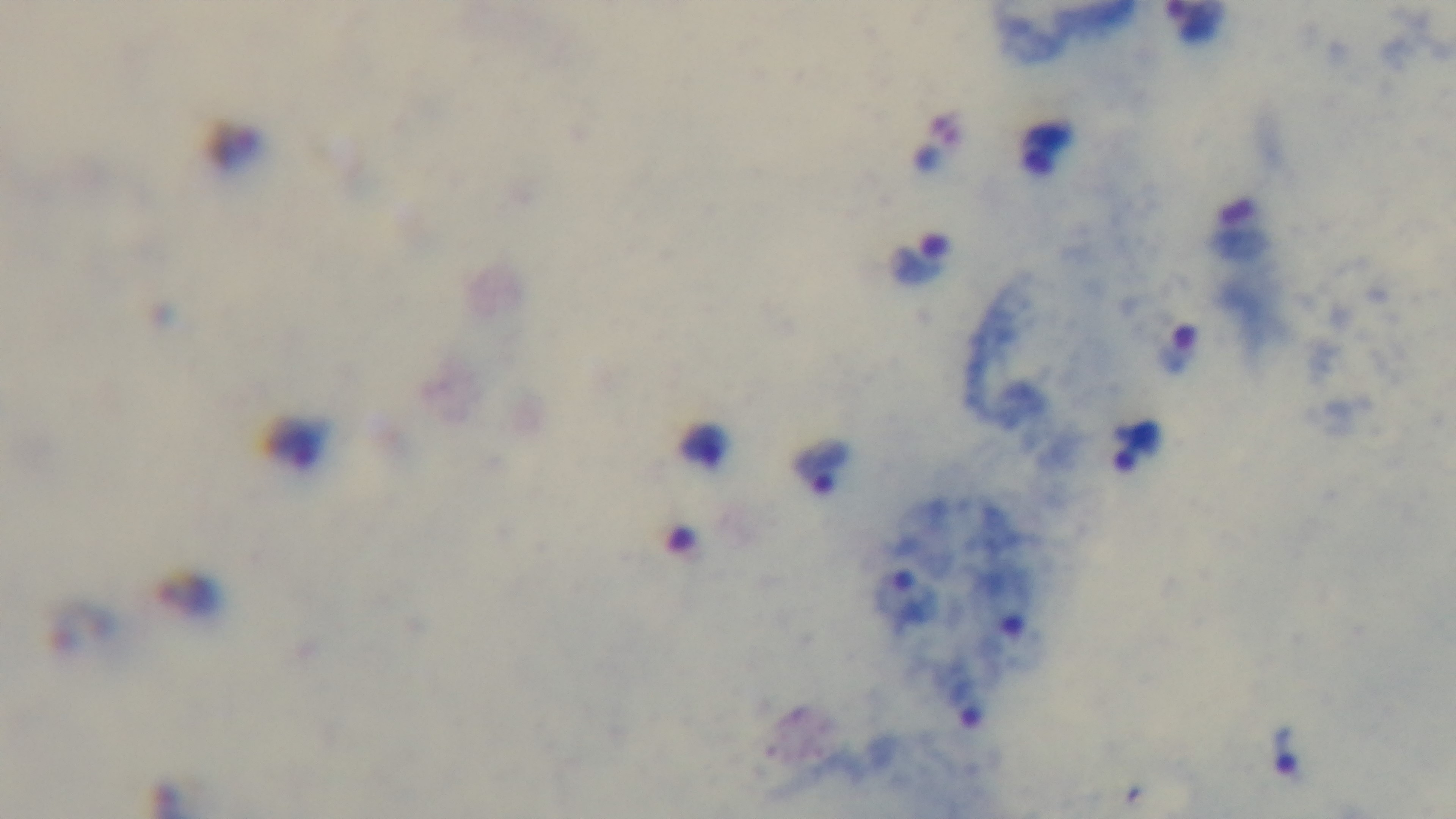
Summary:
  - Field of view: one from the slide
  - Objective: 100x oil immersion
  - Capture: mounted 4K digital camera
  - Preparation: thick smear
  - Malaria status: positive
  - Stain: Giemsa
  - Modality: light microscopy